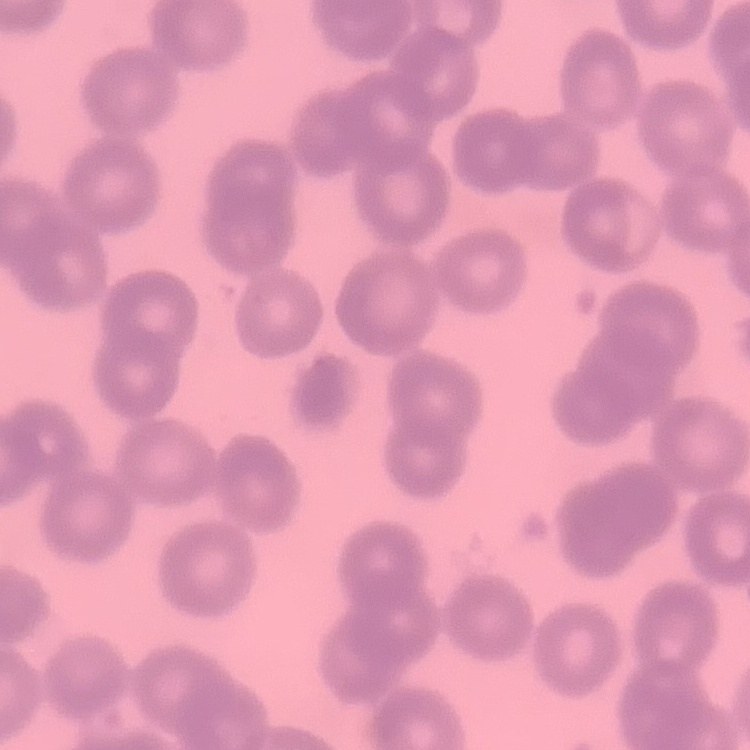 The erythrocytes show no rouleaux formation. Square crop of a larger photomicrograph. Thin peripheral smear. Field's or Giemsa stain.